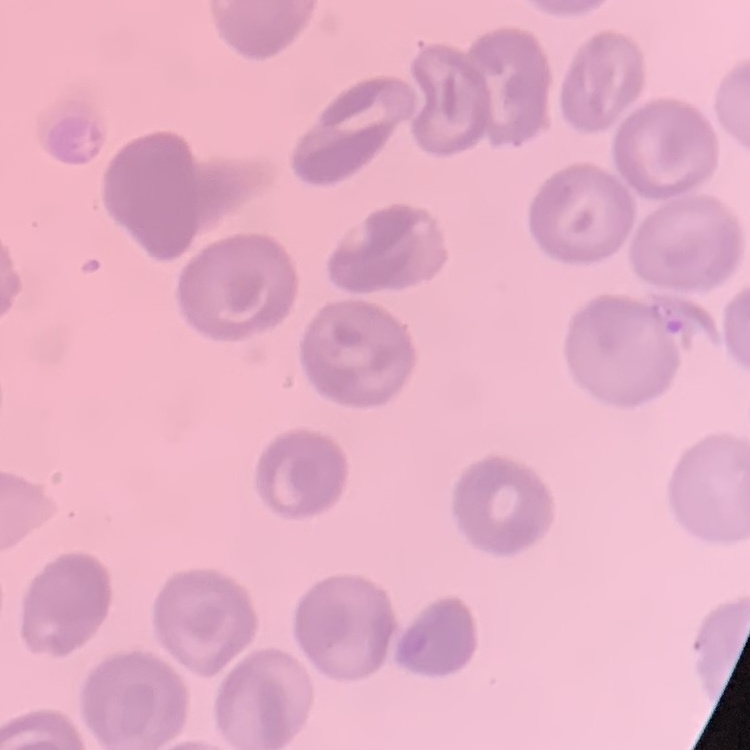
red blood cell morphology = no rouleaux formation
preparation = thin peripheral smear
image type = square crop of a larger photomicrograph
stain = Field's or Giemsa